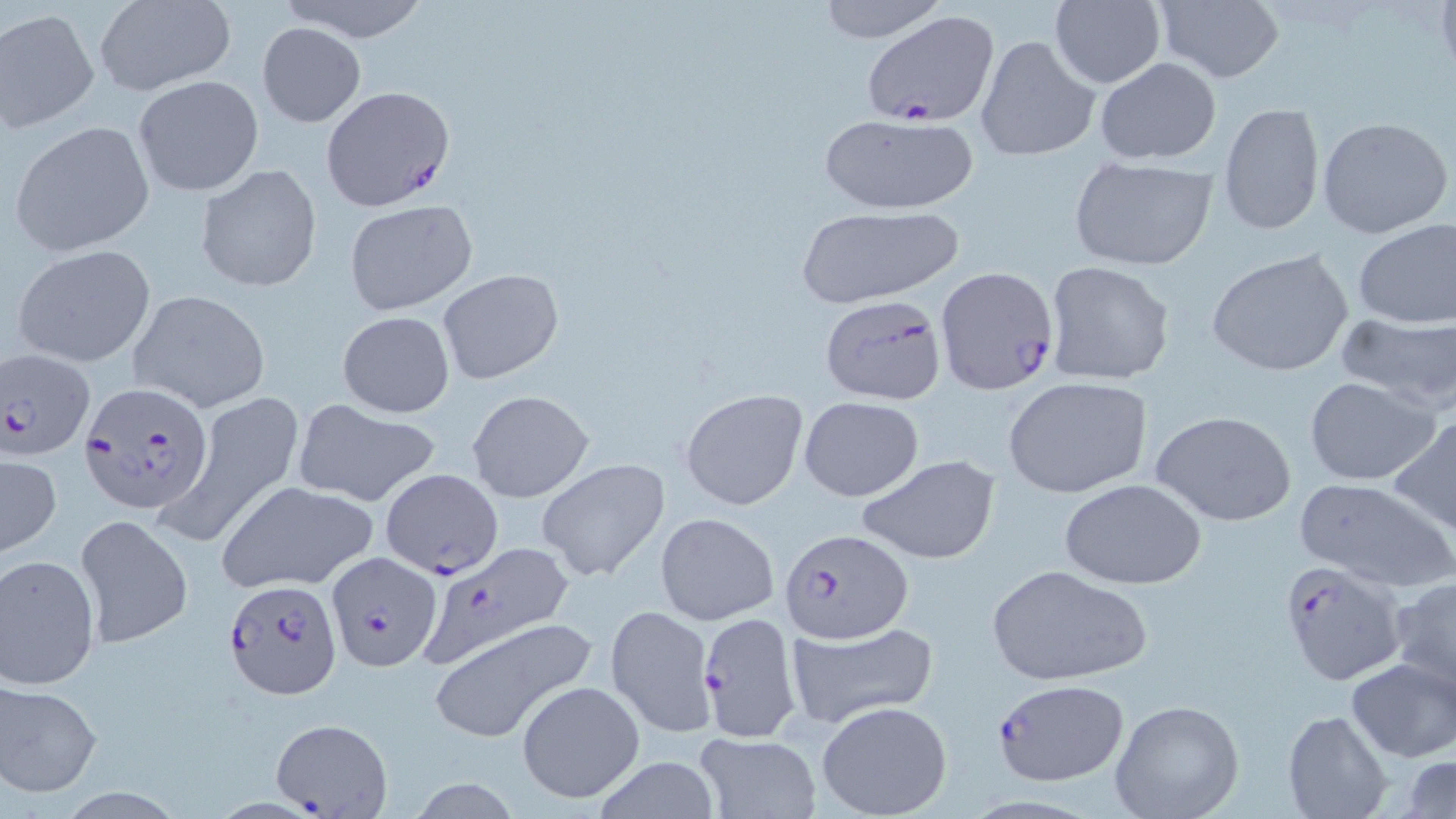

Summary:
  - Coordinate format: approximate bounding boxes as named x1/y1/x2/y2 corners in pixels
  - Uninfected red blood cell locations: (x1=273, y1=0, x2=431, y2=43), (x1=812, y1=0, x2=951, y2=44), (x1=1151, y1=1, x2=1288, y2=84), (x1=93, y1=2, x2=236, y2=96), (x1=1049, y1=2, x2=1166, y2=88), (x1=1, y1=9, x2=99, y2=133), (x1=256, y1=22, x2=367, y2=127), (x1=975, y1=33, x2=1099, y2=163), (x1=1094, y1=57, x2=1221, y2=165), (x1=136, y1=75, x2=262, y2=196), (x1=1219, y1=101, x2=1325, y2=237), (x1=815, y1=111, x2=983, y2=216), (x1=1316, y1=116, x2=1455, y2=241), (x1=8, y1=121, x2=155, y2=257), (x1=1067, y1=160, x2=1217, y2=270), (x1=196, y1=163, x2=322, y2=291), (x1=342, y1=199, x2=478, y2=316), (x1=794, y1=206, x2=965, y2=307), (x1=1352, y1=218, x2=1456, y2=330), (x1=10, y1=243, x2=156, y2=368), (x1=1205, y1=248, x2=1355, y2=378), (x1=1043, y1=260, x2=1175, y2=388), (x1=437, y1=269, x2=565, y2=385), (x1=128, y1=288, x2=272, y2=412), (x1=337, y1=311, x2=455, y2=418), (x1=1334, y1=312, x2=1456, y2=412), (x1=1004, y1=377, x2=1153, y2=498), (x1=1304, y1=377, x2=1440, y2=484), (x1=679, y1=388, x2=808, y2=510), (x1=467, y1=390, x2=595, y2=502), (x1=162, y1=391, x2=303, y2=550), (x1=799, y1=395, x2=925, y2=501), (x1=293, y1=399, x2=442, y2=507), (x1=1151, y1=409, x2=1299, y2=527), (x1=1387, y1=415, x2=1456, y2=533), (x1=1, y1=451, x2=62, y2=559), (x1=857, y1=455, x2=999, y2=565), (x1=538, y1=458, x2=670, y2=582), (x1=381, y1=467, x2=504, y2=578), (x1=1057, y1=477, x2=1207, y2=590), (x1=1294, y1=478, x2=1455, y2=593), (x1=216, y1=480, x2=378, y2=593), (x1=654, y1=511, x2=779, y2=626), (x1=75, y1=514, x2=192, y2=648), (x1=0, y1=553, x2=101, y2=689), (x1=985, y1=564, x2=1153, y2=686), (x1=1387, y1=578, x2=1456, y2=698), (x1=606, y1=604, x2=715, y2=738), (x1=425, y1=617, x2=596, y2=744), (x1=783, y1=621, x2=939, y2=728), (x1=464, y1=639, x2=627, y2=788), (x1=1346, y1=658, x2=1455, y2=763), (x1=1, y1=679, x2=102, y2=796), (x1=515, y1=679, x2=646, y2=806), (x1=1108, y1=699, x2=1245, y2=819), (x1=815, y1=700, x2=952, y2=818), (x1=1283, y1=709, x2=1393, y2=819), (x1=693, y1=732, x2=822, y2=818), (x1=587, y1=754, x2=725, y2=819), (x1=1404, y1=757, x2=1456, y2=817)
  - Plasmodium falciparum-infected red blood cell locations: (x1=861, y1=10, x2=1000, y2=127), (x1=322, y1=87, x2=455, y2=210), (x1=935, y1=267, x2=1058, y2=394), (x1=817, y1=294, x2=946, y2=405), (x1=1, y1=349, x2=96, y2=460), (x1=82, y1=382, x2=214, y2=515), (x1=778, y1=527, x2=910, y2=642), (x1=417, y1=543, x2=571, y2=663), (x1=326, y1=552, x2=441, y2=670), (x1=1278, y1=559, x2=1407, y2=685), (x1=225, y1=580, x2=341, y2=697), (x1=699, y1=613, x2=801, y2=742), (x1=989, y1=678, x2=1129, y2=787), (x1=271, y1=715, x2=393, y2=816)
  - Slide-level diagnosis: Plasmodium falciparum
  - Field of view: single
  - Stain: May-Grünwald-Giemsa
  - Modality: light microscopy
  - Magnification: 1000x
  - Preparation: thin blood smear
  - Image size: 1456×819 pixels